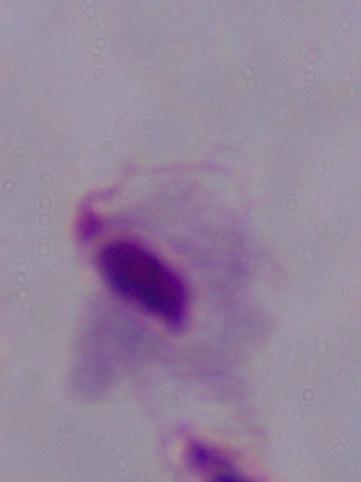
A trichomonad is shown. Micrograph. 1000x magnification.